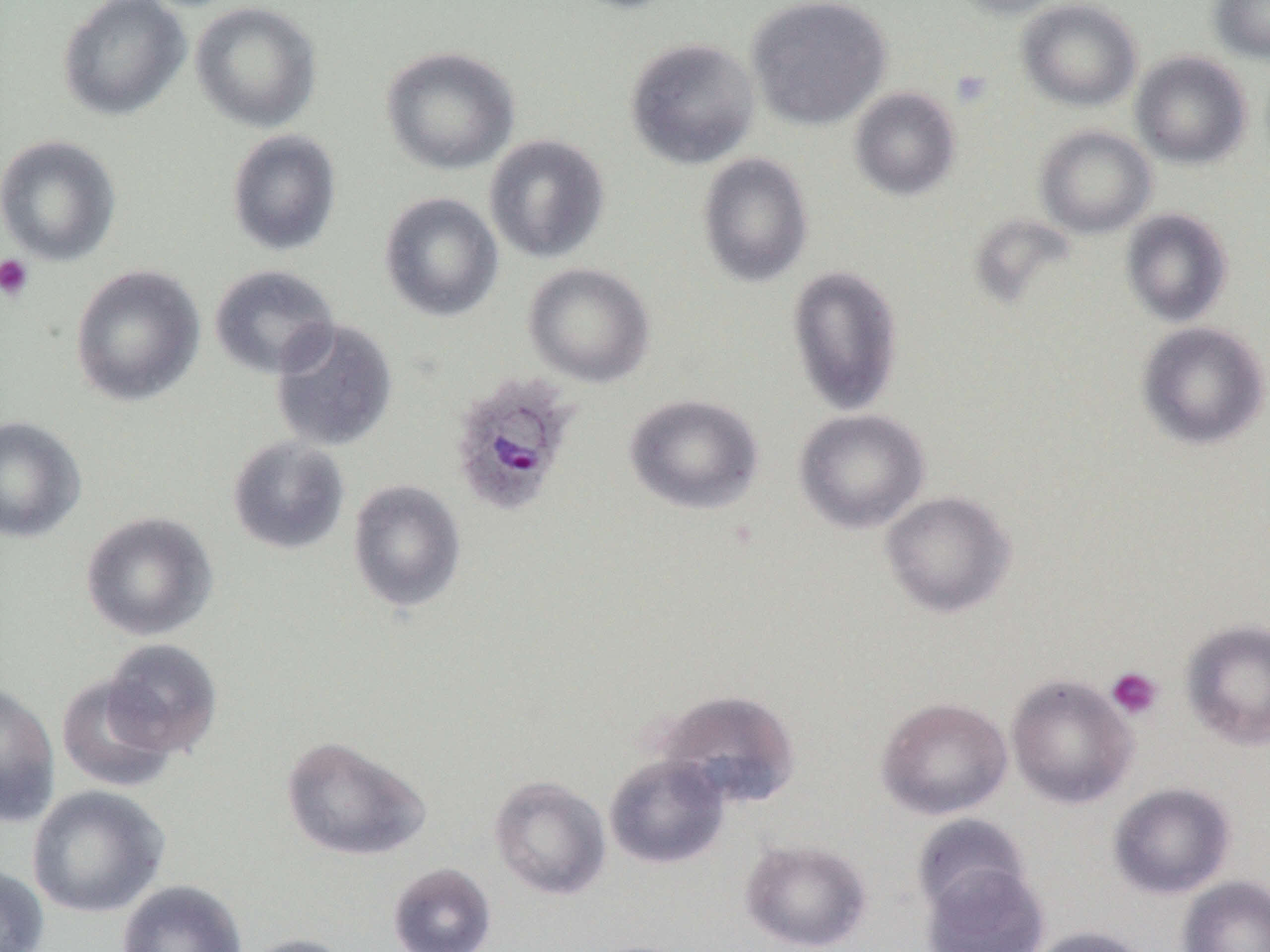
Summary:
  - Coordinate format: approximate bounding boxes as [x1, y1, x2, y2] in pixels
  - Plasmodium ovale-infected red blood cell locations: [448, 373, 579, 517]
  - Uninfected red blood cell locations: [57, 0, 191, 122], [560, 0, 687, 14], [746, 0, 892, 130], [948, 0, 1070, 19], [1017, 0, 1142, 111], [1208, 0, 1270, 64], [190, 1, 322, 133], [624, 37, 760, 169], [380, 45, 520, 175], [1130, 51, 1252, 169], [849, 86, 961, 201], [1034, 125, 1156, 238], [227, 129, 342, 256], [484, 134, 610, 264], [0, 135, 121, 266], [697, 153, 813, 288], [379, 192, 503, 322], [1120, 208, 1233, 327], [523, 262, 655, 388], [69, 264, 205, 407], [208, 264, 340, 380], [786, 265, 904, 416], [270, 318, 399, 452], [1136, 321, 1269, 450], [623, 393, 764, 515], [794, 409, 930, 534], [0, 415, 87, 543], [226, 436, 351, 555], [347, 479, 466, 613], [880, 490, 1016, 618], [80, 511, 219, 641], [1180, 619, 1270, 750], [101, 638, 223, 757], [55, 674, 177, 793], [1007, 674, 1138, 809], [0, 681, 61, 827], [655, 689, 801, 809], [875, 696, 1013, 819], [280, 734, 431, 862], [604, 753, 730, 869], [489, 774, 611, 900], [1108, 782, 1236, 899], [27, 785, 170, 918], [911, 814, 1032, 918], [739, 837, 873, 951], [388, 861, 496, 952], [921, 863, 1050, 952], [0, 864, 49, 952], [1177, 875, 1270, 952], [116, 880, 248, 952], [1027, 925, 1150, 952], [239, 933, 357, 952]
  - Platelet locations: [950, 68, 993, 108], [0, 254, 34, 302], [1106, 666, 1163, 720]
  - Slide-level diagnosis: Plasmodium ovale
  - Magnification: 1000x
  - Preparation: thin blood film
  - Field of view: one of a larger specimen
  - Image size: 1270×952 pixels
  - Modality: optical microscopy